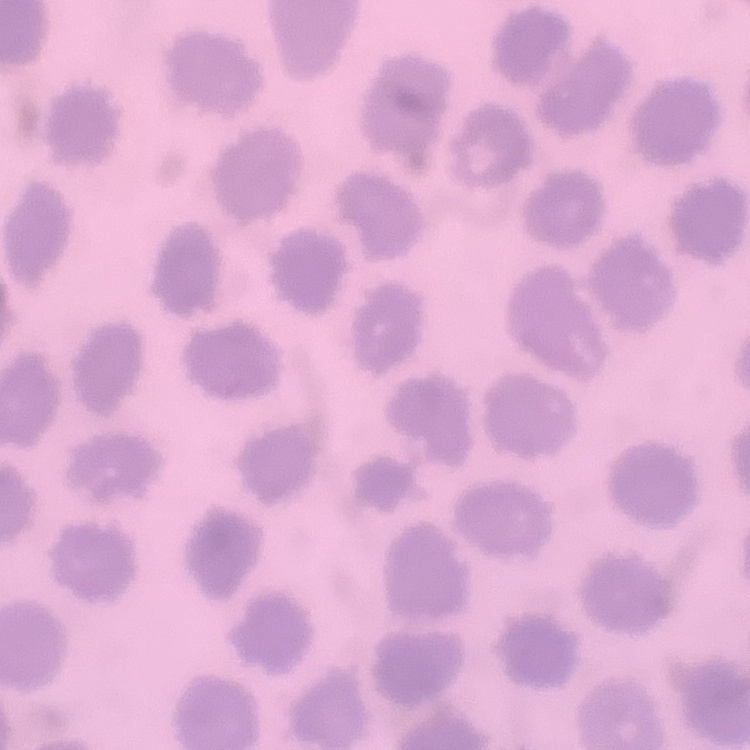
erythrocyte_morphology: no rouleaux formation
stain: Field's or Giemsa
preparation: thin blood film
image_type: one tile cut from a larger photomicrograph